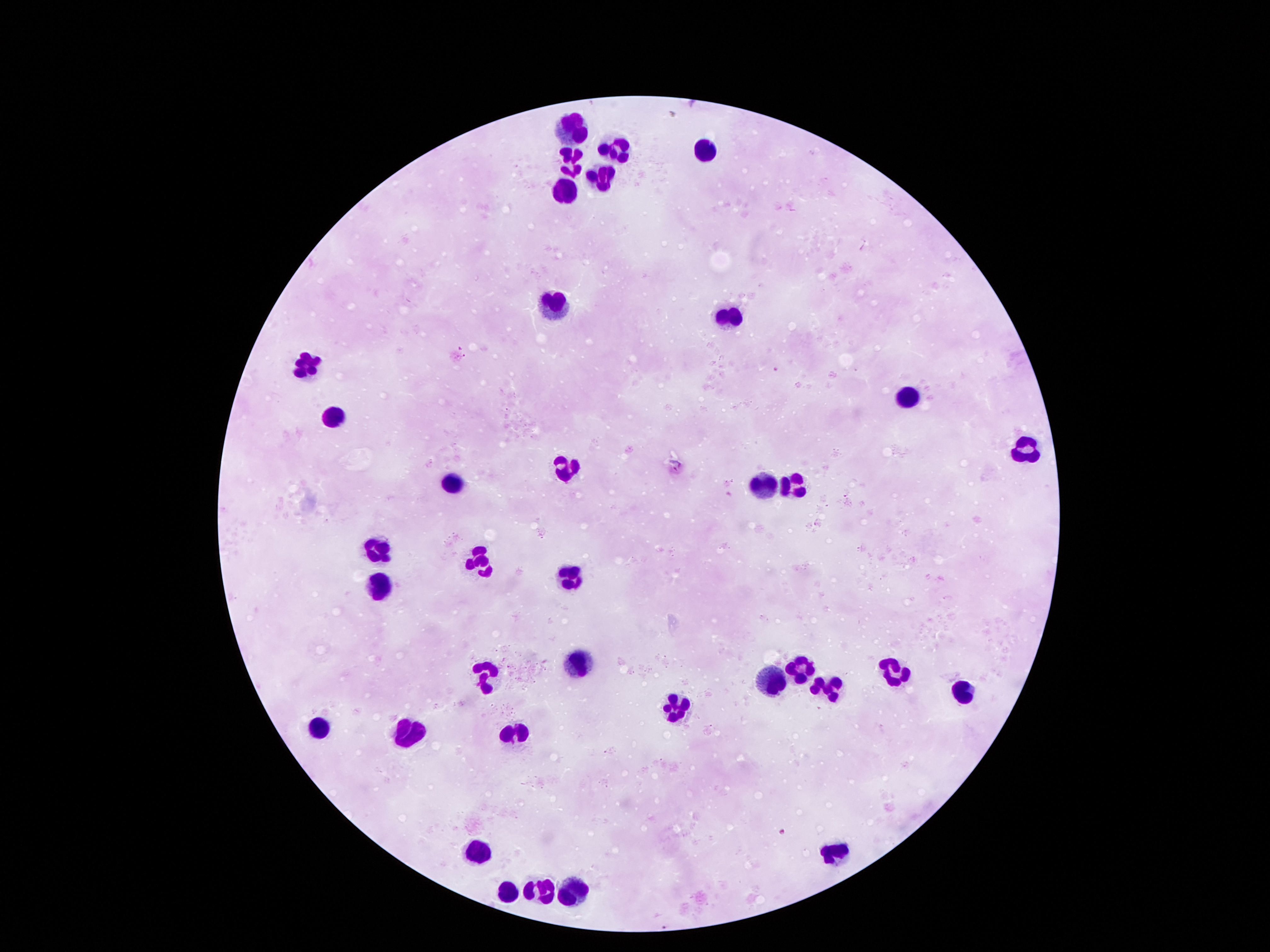
leukocyte locations = approximate centers as (x, y) in pixels: (575, 128), (614, 145), (703, 151), (573, 160), (600, 186), (562, 191), (555, 304), (733, 317), (310, 363), (905, 401), (335, 413), (1025, 459), (567, 463), (455, 477), (792, 483), (761, 484), (380, 549), (481, 563), (574, 572), (383, 590), (580, 658), (798, 667), (892, 667), (486, 678), (767, 680), (827, 690), (963, 692), (673, 707), (319, 724), (407, 730), (512, 734), (838, 846), (471, 849), (536, 888), (507, 889), (573, 890)
preparation = thick blood smear
magnification = 100x
patient malaria status = negative
capture = smartphone camera through the microscope eyepiece
image size = 1270×952 pixels
field of view = single
stain = Giemsa